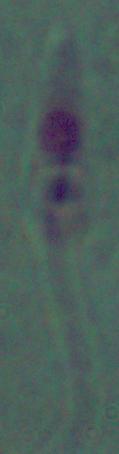
Micrograph. A Leishmania parasite is shown. Captured at 1000x magnification.